Name the parasite shown.
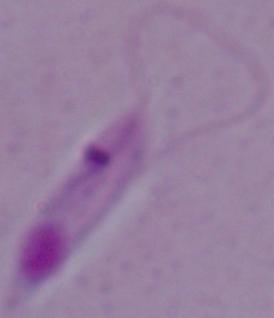

This is Leishmania.

Micrograph. 1000x magnification.